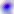

{
  "identification": "Toxoplasma gondii",
  "magnification": "400x",
  "modality": "photomicrograph"
}